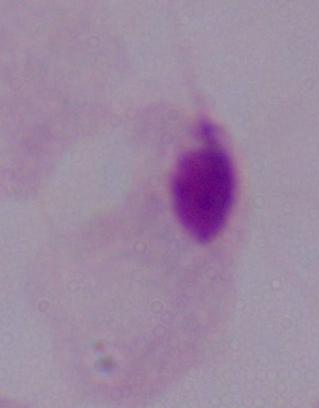
identification = trichomonad
magnification = 1000x
modality = micrograph